Report the malaria status of this cell.
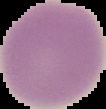
It is uninfected.

The area outside the segmented cell region is set to black. Image is 106×109 pixels. From a thin blood smear.